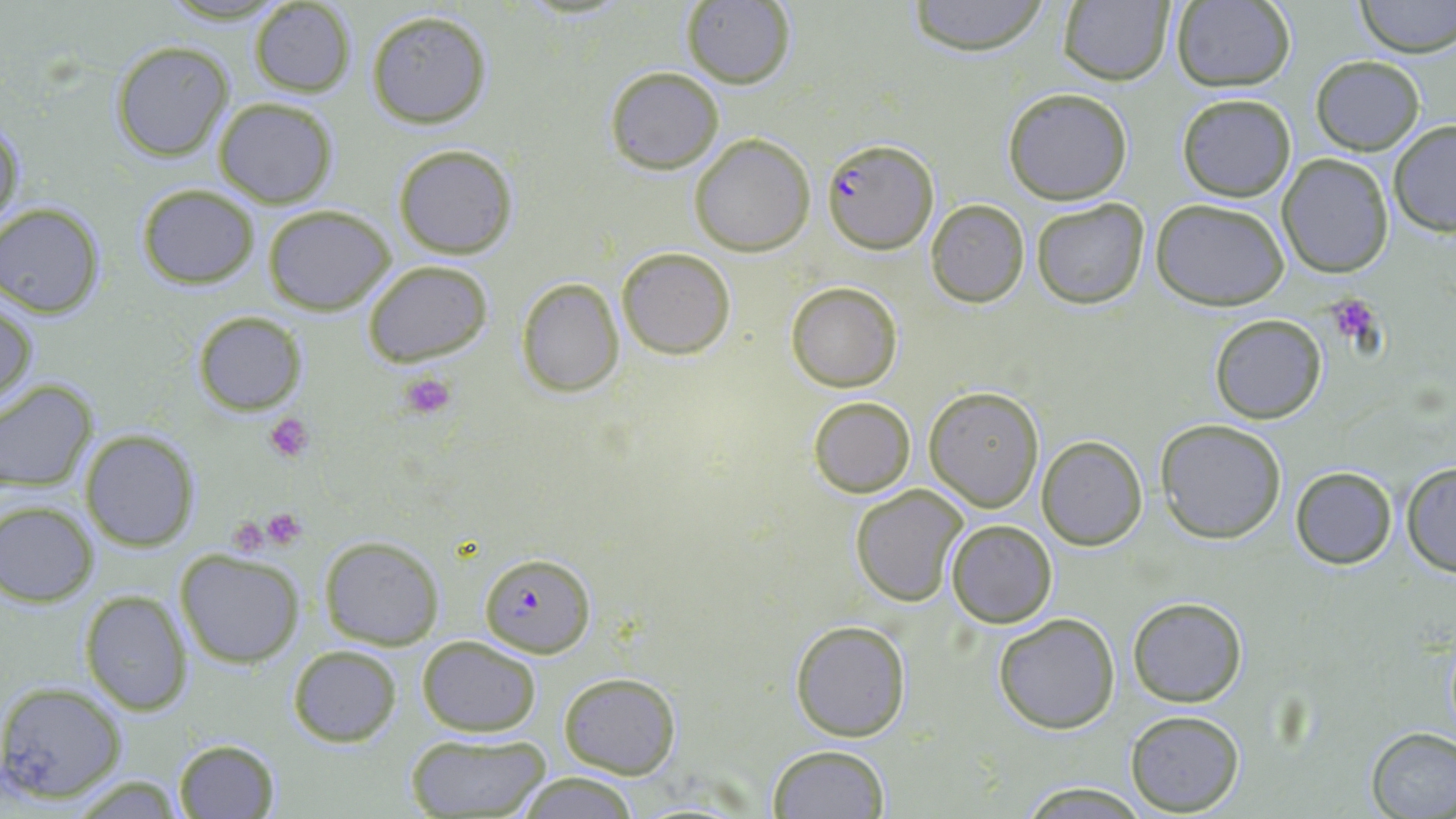
Summary:
  - Coordinate format: approximate bounding boxes as [x1, y1, x2, y2] in pixels
  - Uninfected red blood cell locations: [904, 0, 1053, 55], [1058, 0, 1174, 85], [1356, 0, 1456, 57], [247, 1, 358, 96], [1169, 1, 1296, 92], [679, 2, 796, 88], [366, 10, 493, 128], [112, 40, 236, 162], [1311, 56, 1424, 154], [605, 66, 723, 173], [1003, 88, 1133, 205], [1176, 93, 1296, 202], [212, 98, 338, 208], [1, 115, 23, 231], [1389, 121, 1456, 237], [689, 132, 816, 257], [393, 143, 518, 259], [1277, 153, 1393, 278], [137, 184, 260, 289], [926, 199, 1030, 307], [1031, 199, 1148, 309], [1152, 200, 1289, 310], [263, 204, 395, 315], [0, 205, 106, 318], [616, 246, 736, 359], [362, 259, 494, 365], [516, 277, 625, 398], [786, 282, 902, 391], [1, 296, 37, 411], [193, 311, 306, 416], [1209, 314, 1326, 424], [0, 381, 98, 492], [924, 387, 1044, 512], [807, 396, 917, 496], [1156, 420, 1287, 543], [79, 428, 201, 551], [1037, 435, 1146, 551], [1400, 462, 1456, 576], [1290, 466, 1397, 569], [849, 484, 970, 607], [0, 502, 100, 606], [946, 520, 1057, 628], [318, 535, 444, 649], [174, 548, 306, 667], [78, 590, 193, 716], [1128, 597, 1247, 707], [992, 612, 1121, 733], [790, 620, 911, 740], [416, 637, 542, 736], [287, 645, 402, 747], [558, 672, 681, 778], [0, 680, 128, 804], [1125, 710, 1246, 816], [1367, 726, 1456, 819], [405, 732, 551, 817], [172, 738, 283, 819], [767, 744, 890, 818], [514, 770, 641, 819], [63, 775, 192, 815], [1015, 782, 1151, 816]
  - Platelet locations: [1327, 295, 1382, 345], [398, 372, 458, 421], [264, 414, 312, 464], [260, 508, 307, 547], [231, 521, 265, 561]
  - Plasmodium falciparum-infected red blood cell locations: [822, 136, 938, 255], [479, 551, 594, 656]
  - Slide-level diagnosis: Plasmodium falciparum
  - Field of view: single
  - Preparation: thin blood film
  - Modality: optical microscopy
  - Image size: 1456×819 pixels
  - Stain: May-Grünwald-Giemsa
  - Magnification: 1000x